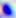

magnification = 400x
modality = micrograph
identification = Toxoplasma gondii